Describe the morphology of the red blood cells.
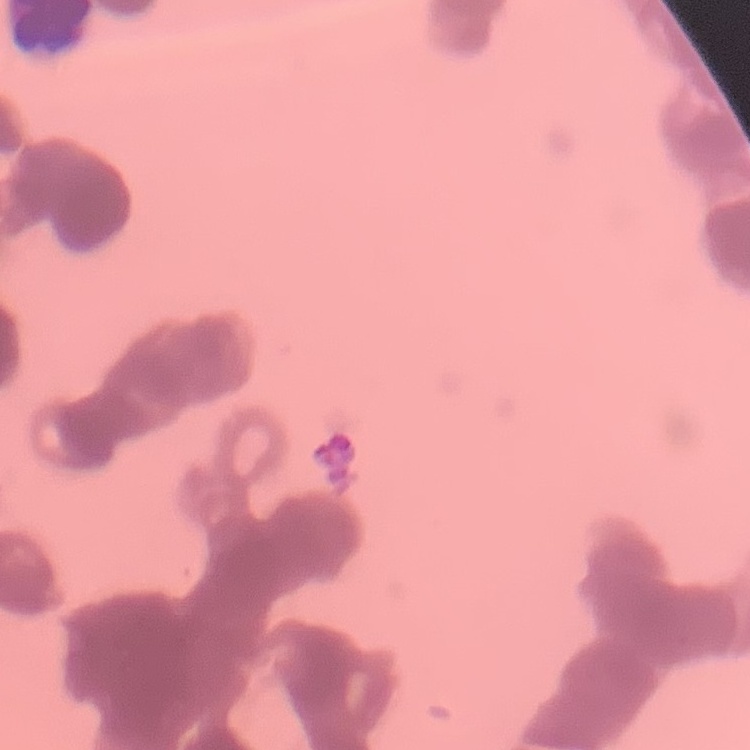
They show rouleaux formation.

One tile cut from a larger photomicrograph. Thin blood film. Stained with either Field's or Giemsa.